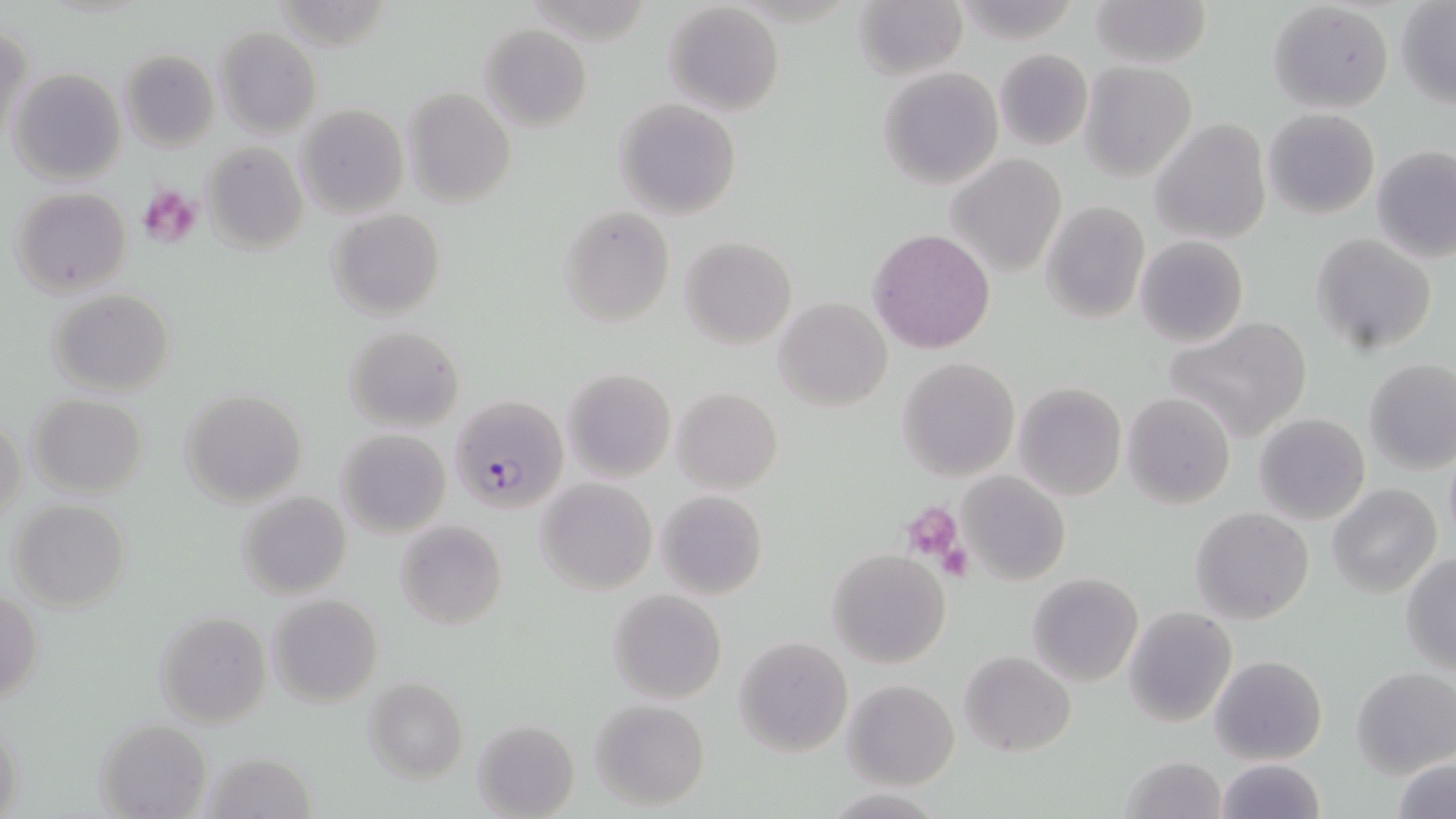

{
  "slide_level_diagnosis": "Plasmodium falciparum",
  "stain": "May-Grünwald-Giemsa",
  "platelet_locations": "approximate bounding boxes as (x1,y1)-(x2,y2) corner pairs in pixels: (136,184)-(200,246), (903,506)-(964,567), (939,542)-(975,582)",
  "image_size": "1456×819 pixels",
  "modality": "light microscopy",
  "uninfected_red_blood_cell_locations": "approximate bounding boxes as (x1,y1)-(x2,y2) corner pairs in pixels: (1090,0)-(1210,69), (853,1)-(968,79), (1268,2)-(1394,114), (662,3)-(786,115), (1396,3)-(1456,108), (480,24)-(592,132), (1,26)-(31,142), (215,27)-(321,136), (992,48)-(1093,151), (119,49)-(219,152), (1080,62)-(1196,181), (877,67)-(1003,188), (9,68)-(127,185), (402,87)-(516,208), (615,98)-(741,220), (296,104)-(408,218), (1262,108)-(1380,219), (1150,118)-(1272,245), (200,142)-(308,253), (1372,145)-(1456,262), (946,154)-(1068,278), (10,186)-(132,296), (1040,200)-(1150,324), (559,205)-(676,326), (327,208)-(446,319), (868,227)-(997,355), (1309,234)-(1437,356), (680,236)-(796,348), (1135,236)-(1248,348), (48,290)-(175,396), (774,297)-(892,410), (1165,315)-(1314,443), (343,325)-(465,431), (897,356)-(1019,480), (1364,359)-(1456,474), (562,368)-(677,481), (1013,382)-(1126,500), (672,388)-(782,494), (180,389)-(307,508), (1122,391)-(1235,509), (27,394)-(148,497), (1253,412)-(1371,525), (1,414)-(26,526), (337,427)-(451,538), (1444,451)-(1456,547), (957,471)-(1070,585), (536,477)-(657,595), (1328,484)-(1441,598), (654,490)-(769,600), (237,491)-(351,600), (8,499)-(130,612), (1191,507)-(1314,624), (395,519)-(506,630), (828,548)-(951,668), (1401,553)-(1456,674), (1026,573)-(1143,686), (1,587)-(43,711), (607,589)-(727,706), (268,594)-(383,707), (1124,606)-(1237,727), (154,612)-(270,728), (734,637)-(853,756), (960,651)-(1076,756), (1210,655)-(1328,764), (1351,666)-(1456,778), (364,677)-(467,782), (843,679)-(960,789), (589,699)-(710,810), (1,713)-(25,819), (96,719)-(212,817), (471,719)-(579,818), (1391,751)-(1455,818), (1119,755)-(1230,818), (1215,759)-(1324,818)",
  "preparation": "thin blood smear",
  "magnification": "1000x",
  "plasmodium_falciparum_infected_red_blood_cell_locations": "approximate bounding boxes as (x1,y1)-(x2,y2) corner pairs in pixels: (450,394)-(568,510)",
  "field_of_view": "one of a larger specimen"
}